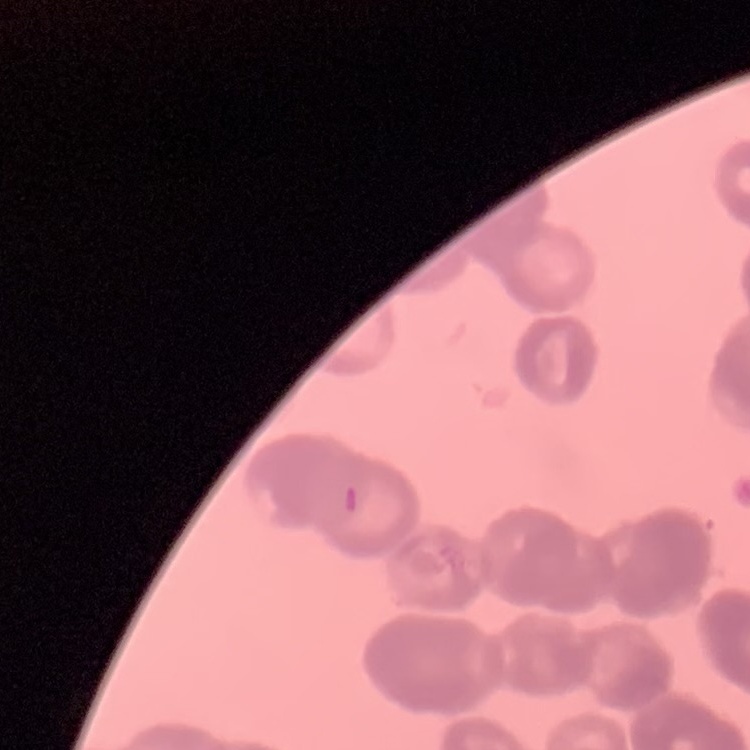

Summary:
  - Red blood cell morphology: rouleaux formation
  - Stain: Field's or Giemsa
  - Image type: square crop of a larger photomicrograph
  - Preparation: thin blood film